Locate every Plasmodium falciparum-infected red blood cell.
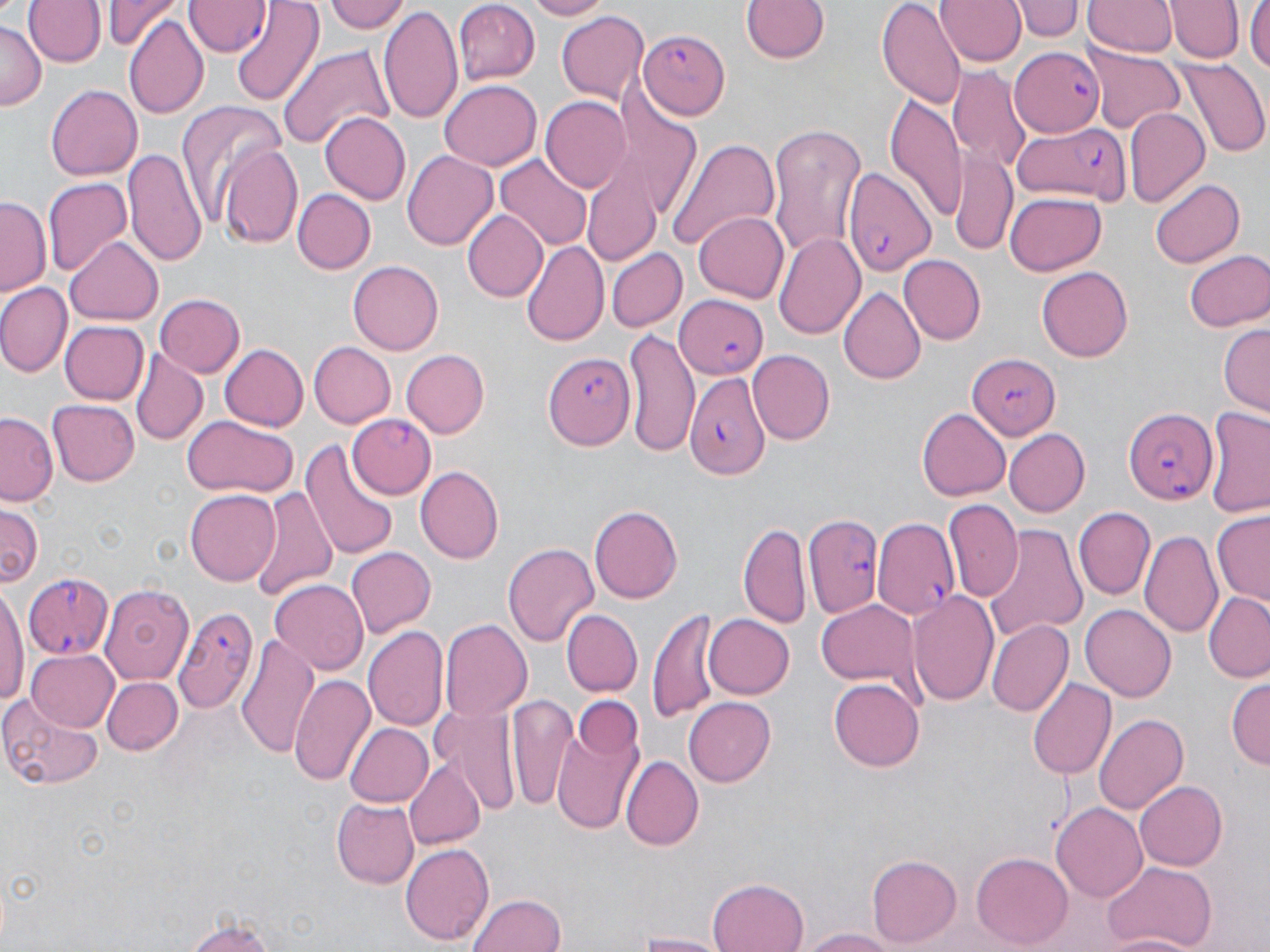

Approximate bounding boxes as (x1, y1, x2, y2) in pixels.
Plasmodium falciparum-infected red blood cells: (185, 0, 272, 57), (639, 29, 728, 119), (1012, 46, 1103, 134), (1011, 120, 1131, 207), (843, 165, 935, 275), (672, 290, 767, 382), (543, 353, 634, 449), (967, 354, 1057, 439), (684, 370, 766, 478), (1123, 407, 1215, 505), (345, 415, 436, 500), (806, 512, 886, 615), (873, 520, 958, 620), (22, 572, 115, 660), (174, 606, 256, 713).

Uninfected red blood cell locations: (23, 0, 105, 68), (105, 0, 176, 49), (232, 0, 321, 107), (327, 0, 409, 35), (521, 0, 609, 20), (740, 0, 829, 66), (878, 0, 965, 110), (936, 0, 1022, 69), (1016, 0, 1081, 43), (1083, 0, 1177, 58), (1166, 0, 1244, 65), (1247, 0, 1270, 76), (455, 3, 540, 84), (379, 5, 463, 123), (556, 11, 651, 104), (125, 15, 208, 119), (1, 22, 46, 110), (279, 43, 395, 148), (1088, 47, 1185, 133), (1177, 61, 1267, 156), (951, 68, 1027, 167), (440, 81, 542, 170), (47, 83, 145, 180), (540, 96, 630, 190), (885, 97, 969, 218), (176, 98, 285, 227), (1124, 106, 1210, 210), (319, 112, 411, 204), (768, 128, 868, 260), (667, 137, 782, 250), (221, 143, 304, 249), (125, 145, 208, 270), (403, 150, 499, 253), (948, 152, 1018, 254), (497, 156, 592, 252), (584, 165, 661, 268), (43, 176, 132, 275), (1151, 178, 1245, 268), (294, 189, 374, 273), (1004, 192, 1106, 276), (0, 198, 48, 295), (461, 209, 546, 301), (693, 211, 788, 303), (774, 232, 865, 339), (66, 237, 165, 326), (521, 241, 610, 348), (607, 248, 686, 332), (1184, 249, 1269, 333), (900, 256, 986, 345), (350, 259, 445, 355), (1038, 266, 1132, 362), (0, 283, 71, 376), (839, 285, 925, 383), (154, 293, 244, 377), (60, 320, 147, 403), (1218, 321, 1270, 416), (623, 327, 701, 460), (309, 342, 395, 428), (218, 344, 308, 431), (131, 350, 208, 443), (748, 350, 835, 443), (402, 351, 489, 436), (47, 399, 140, 486), (917, 408, 1009, 501), (1204, 408, 1270, 517), (0, 413, 58, 504), (181, 417, 297, 499), (1002, 428, 1088, 516), (301, 436, 398, 562), (416, 465, 505, 563), (251, 483, 336, 602), (184, 489, 279, 587), (945, 500, 1021, 602), (590, 505, 684, 604), (0, 506, 42, 587), (1074, 507, 1155, 599), (1211, 512, 1270, 607), (739, 522, 811, 628), (988, 526, 1086, 641), (1141, 527, 1224, 639), (503, 542, 599, 649), (345, 548, 434, 638), (269, 579, 369, 676), (100, 584, 196, 686), (908, 589, 1000, 705), (0, 590, 27, 708), (1204, 592, 1270, 681), (816, 599, 920, 687), (1080, 604, 1177, 701), (649, 606, 723, 723), (563, 610, 642, 696), (702, 613, 794, 700), (988, 619, 1074, 715), (438, 620, 532, 724), (364, 626, 449, 734), (235, 635, 321, 761), (29, 649, 117, 729), (290, 671, 376, 788), (1026, 676, 1116, 782), (102, 677, 182, 755), (829, 678, 926, 772), (1227, 678, 1268, 773), (567, 693, 645, 777), (0, 695, 105, 791), (506, 695, 577, 813), (683, 696, 776, 787), (432, 702, 524, 815), (548, 709, 643, 837), (1094, 712, 1186, 815), (344, 722, 434, 808), (620, 754, 703, 852), (405, 758, 488, 849), (1135, 779, 1226, 871), (330, 797, 417, 887), (1053, 803, 1148, 904), (402, 843, 493, 946), (972, 852, 1073, 949), (866, 854, 961, 948), (1102, 861, 1219, 949), (706, 876, 806, 952), (468, 893, 565, 952), (179, 914, 287, 952), (795, 928, 905, 952), (626, 931, 731, 951), (1102, 933, 1200, 952). Slide-level diagnosis: Plasmodium falciparum. Image is 1270×952 pixels. 1000x magnification. May-Grünwald-Giemsa-stained preparation. Light microscopy. One field of a larger specimen. Thin blood smear.